Locate and identify every blood parasite.
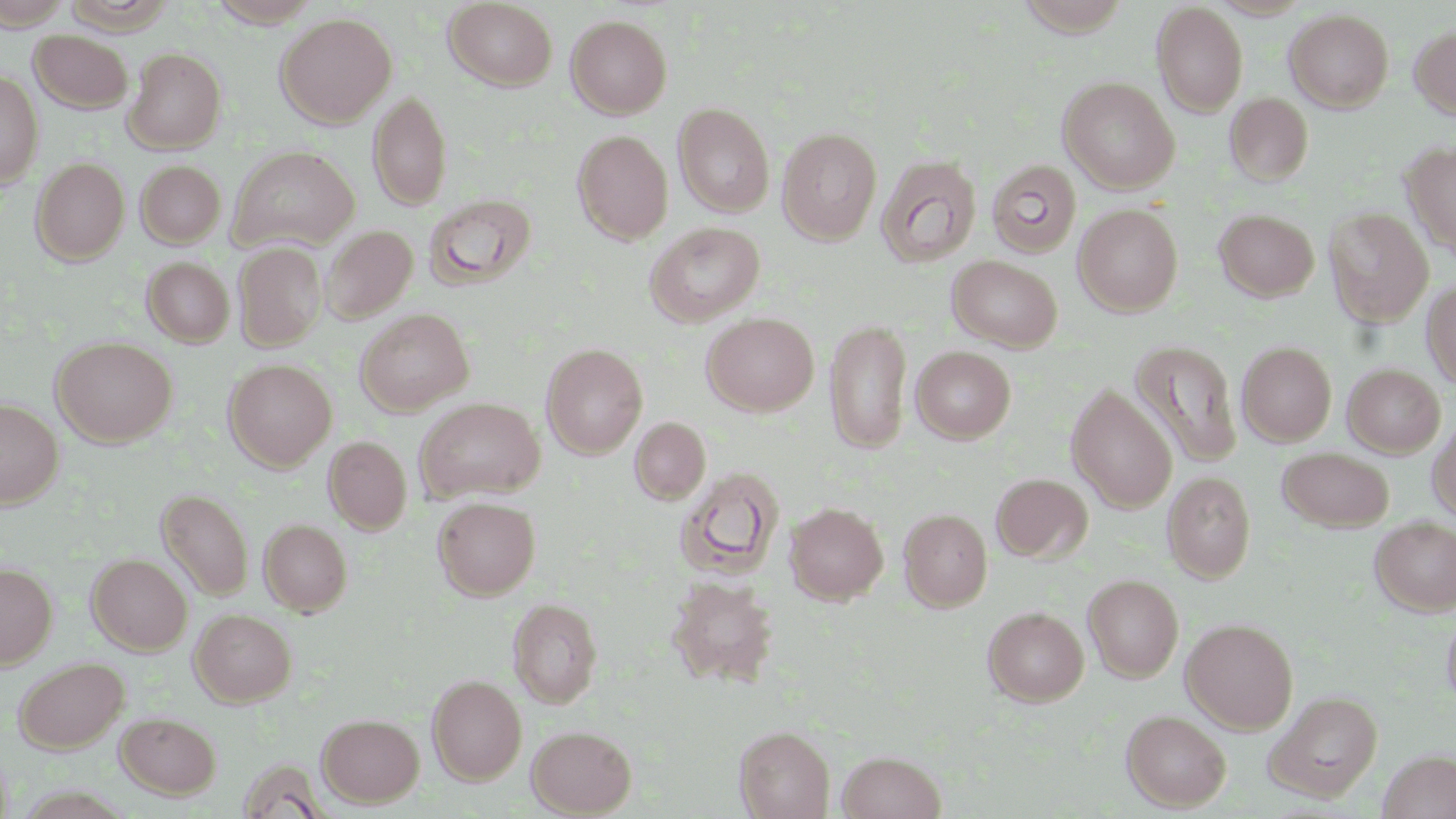

No blood parasites observed.

Summary:
  - Coordinate format: approximate bounding boxes as (x1,y1)-(x2,y2) corner pairs in pixels
  - Uninfected red blood cell locations: (207,0)-(323,28), (1015,0)-(1132,37), (444,1)-(558,90), (1152,3)-(1249,116), (1284,9)-(1394,112), (276,12)-(397,128), (566,15)-(672,119), (1409,24)-(1456,120), (29,30)-(133,112), (124,48)-(226,153), (0,70)-(43,187), (1059,77)-(1179,193), (368,90)-(452,212), (1225,93)-(1314,184), (673,103)-(775,217), (777,127)-(882,244), (572,130)-(674,244), (1401,142)-(1456,259), (228,146)-(360,252), (876,155)-(982,268), (30,157)-(130,265), (986,159)-(1083,258), (135,160)-(226,249), (424,193)-(537,289), (1073,203)-(1184,315), (1323,207)-(1434,327), (1213,208)-(1320,301), (645,221)-(765,327), (321,225)-(418,323), (234,242)-(327,351), (947,255)-(1062,352), (142,257)-(234,347), (1422,279)-(1455,391), (355,308)-(474,416), (701,312)-(819,416), (825,319)-(913,455), (52,337)-(177,447), (1129,339)-(1242,468), (1237,341)-(1337,446), (541,343)-(647,459), (910,346)-(1016,443), (224,359)-(337,470), (1342,363)-(1445,457), (1066,385)-(1178,512), (415,397)-(545,502), (0,399)-(63,508), (1428,415)-(1456,523), (630,417)-(710,505), (324,436)-(412,534), (1277,447)-(1393,531), (675,467)-(785,580), (1162,471)-(1256,583), (991,473)-(1092,562), (156,488)-(253,601), (433,496)-(541,600), (785,502)-(888,604), (898,508)-(992,612), (1371,516)-(1456,615), (259,518)-(352,615), (87,553)-(192,654), (0,563)-(57,669), (1083,574)-(1184,683), (667,576)-(778,688), (507,597)-(603,708), (1441,604)-(1456,711), (983,606)-(1089,706), (190,608)-(296,706), (1181,618)-(1299,733), (13,656)-(129,753), (427,674)-(527,784), (1265,690)-(1383,801), (1121,710)-(1231,811), (115,712)-(221,799), (318,713)-(424,807), (526,725)-(637,816), (734,726)-(834,819), (1377,749)-(1456,818), (836,750)-(947,819)
  - Slide-level diagnosis: negative for blood parasites
  - Stain: May-Grünwald-Giemsa
  - Image size: 1456×819 pixels
  - Magnification: 1000x
  - Field of view: single
  - Modality: light microscopy
  - Preparation: thin blood smear